Comment on the morphology of the red blood cells.
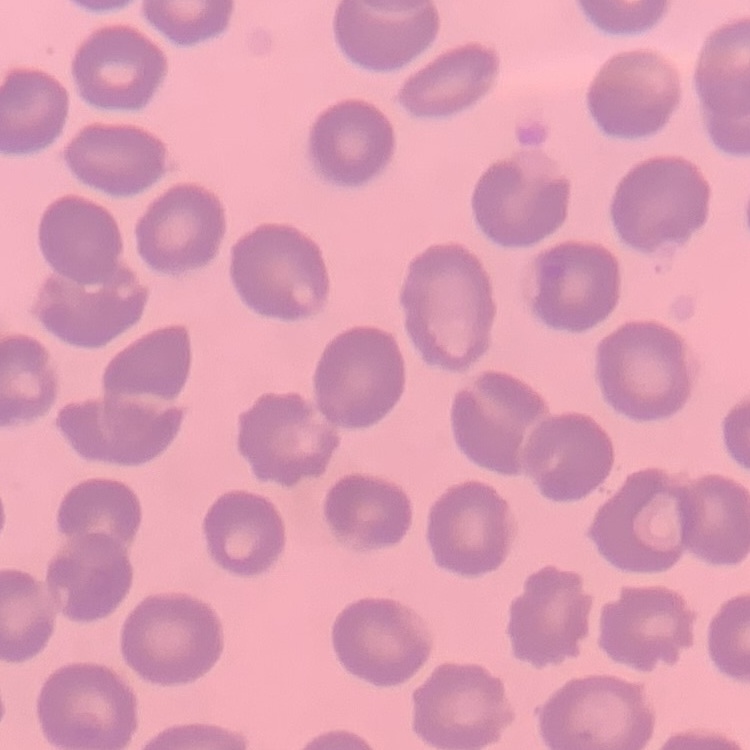

No rouleaux formation.

Summary:
  - Preparation: thin blood smear
  - Stain: Field's or Giemsa
  - Image type: one tile cut from a larger photomicrograph